Report the malaria status of this cell.
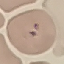

It is uninfected.

stain = Giemsa
image type = automatically extracted cell patch, resized to 64 × 64 pixels
preparation = thin smear
capture = smartphone through the microscope eyepiece